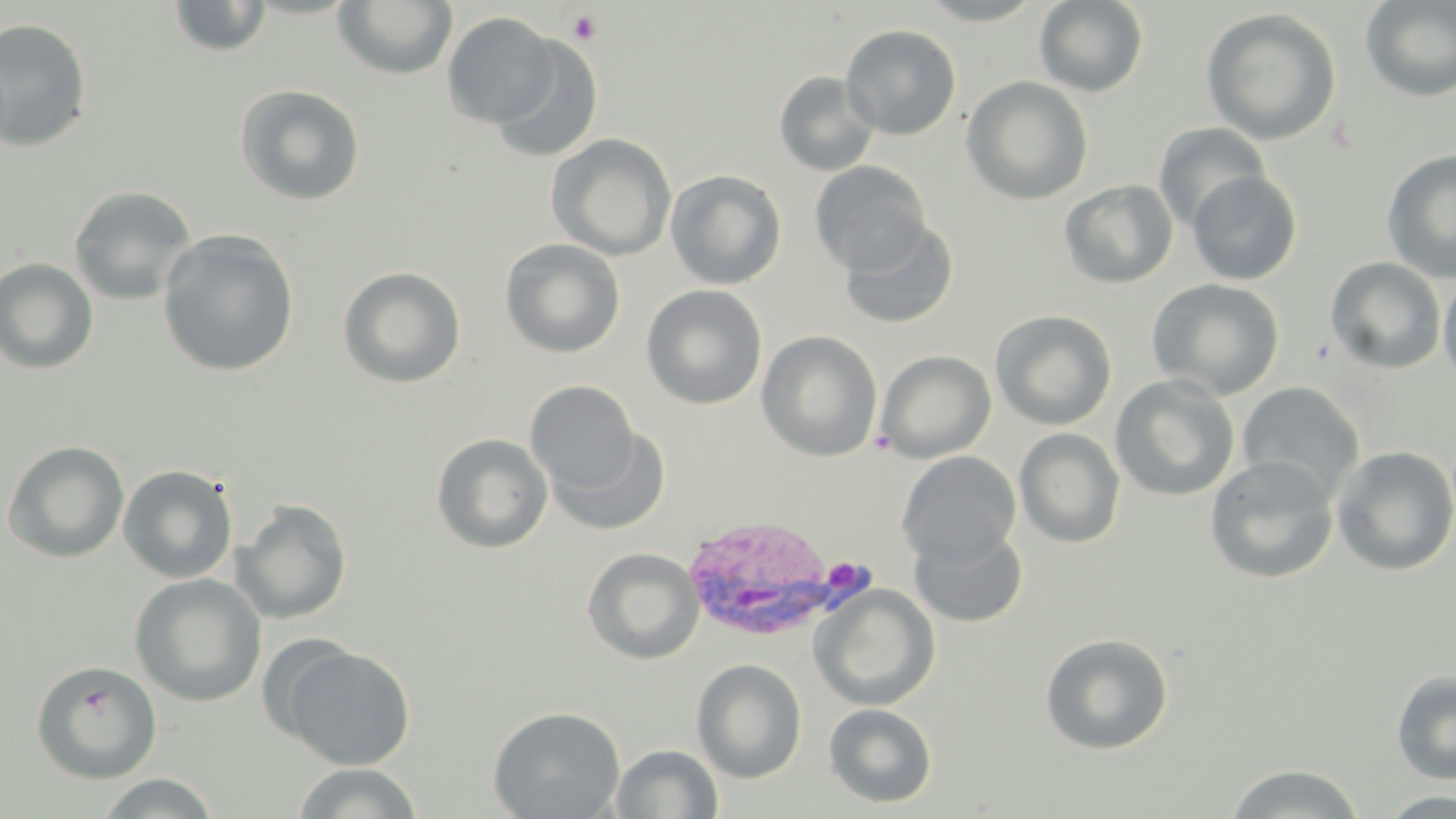

Summary:
  - Coordinate format: approximate bounding boxes as [x1, y1, x2, y2] in pixels
  - Plasmodium vivax-infected red blood cell locations: [678, 516, 872, 644]
  - Platelet locations: [566, 10, 602, 45]
  - Uninfected red blood cell locations: [167, 0, 272, 57], [915, 0, 1049, 25], [1359, 0, 1456, 102], [333, 1, 458, 79], [1034, 1, 1149, 96], [1201, 7, 1342, 145], [443, 12, 560, 128], [0, 18, 93, 152], [841, 24, 961, 140], [489, 38, 605, 163], [773, 70, 880, 177], [962, 76, 1093, 204], [235, 84, 365, 206], [1154, 122, 1270, 230], [547, 133, 677, 260], [1381, 150, 1456, 284], [810, 162, 930, 275], [665, 168, 787, 290], [1187, 170, 1302, 286], [1059, 179, 1178, 289], [69, 185, 197, 305], [839, 219, 956, 328], [158, 230, 299, 377], [500, 239, 625, 358], [1324, 257, 1447, 374], [0, 258, 98, 374], [338, 266, 466, 388], [1438, 270, 1456, 394], [1146, 278, 1285, 401], [641, 284, 767, 410], [990, 309, 1117, 430], [756, 331, 883, 462], [875, 350, 996, 463], [1110, 375, 1240, 501], [525, 380, 640, 496], [1236, 382, 1365, 506], [547, 425, 672, 537], [1014, 428, 1126, 548], [431, 433, 554, 553], [2, 440, 130, 563], [1331, 445, 1456, 577], [896, 452, 1021, 567], [1204, 456, 1340, 585], [118, 464, 238, 583], [233, 498, 352, 624], [909, 525, 1028, 628], [582, 547, 705, 664], [129, 573, 267, 707], [810, 583, 940, 711], [1040, 633, 1173, 754], [277, 643, 416, 769], [692, 658, 807, 783], [31, 661, 162, 784], [1391, 669, 1456, 784], [823, 702, 938, 808], [488, 705, 626, 819], [610, 743, 724, 819], [291, 762, 424, 819], [1224, 763, 1367, 818], [92, 773, 221, 818], [1378, 790, 1456, 817]
  - Slide-level diagnosis: Plasmodium vivax
  - Magnification: 1000x
  - Field of view: single
  - Modality: light microscopy
  - Preparation: thin blood smear
  - Image size: 1456×819 pixels
  - Stain: May-Grünwald-Giemsa